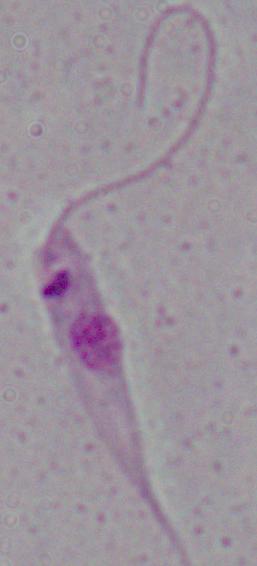
magnification = 1000x
modality = photomicrograph
identification = Leishmania